Find each parasitized red blood cell.
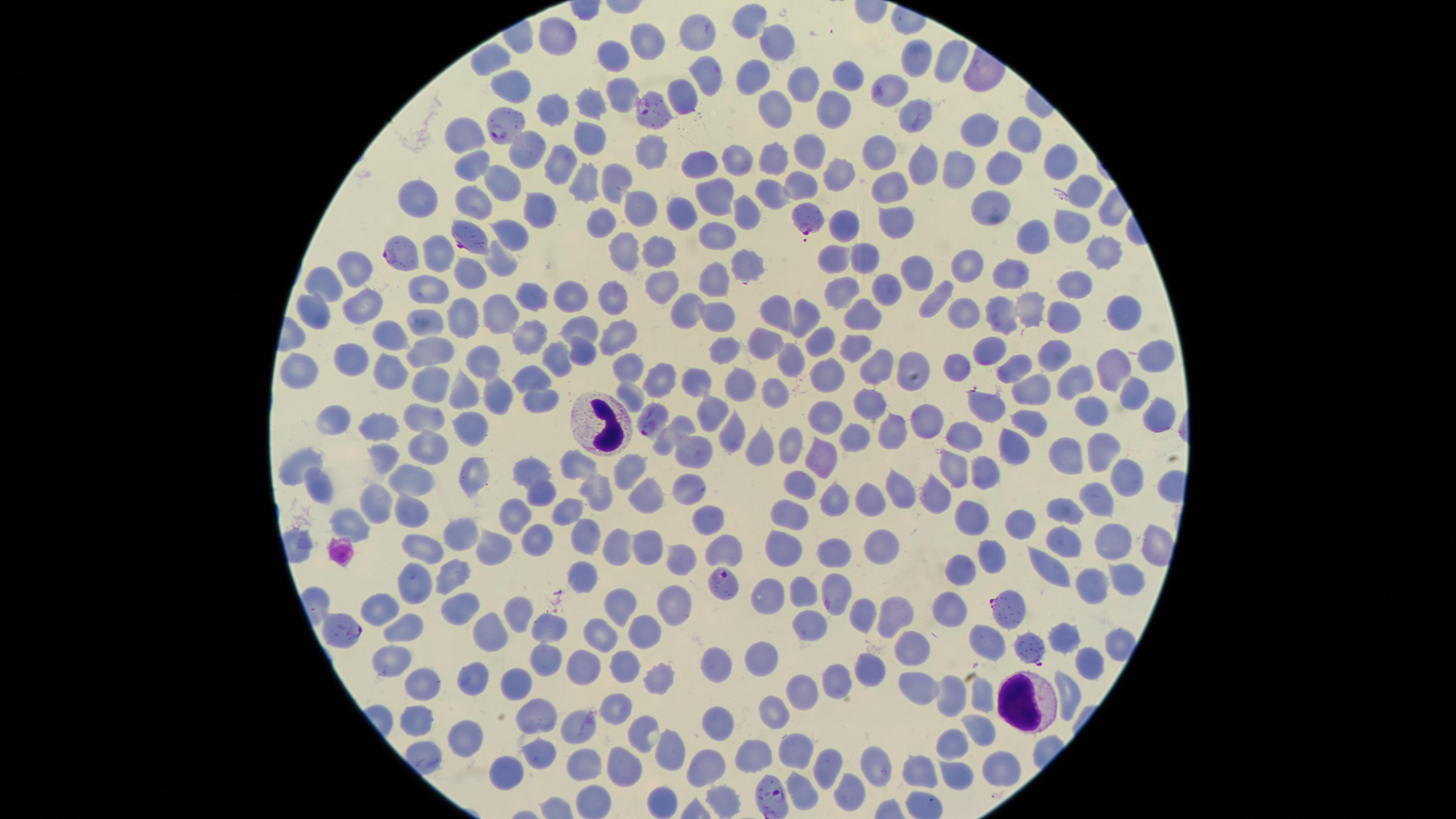

Approximate marker points as {x, y} in pixels.
Parasitized red blood cells: {654, 111}, {506, 126}, {809, 220}, {465, 234}, {397, 256}, {649, 417}, {724, 579}, {1005, 609}, {341, 628}, {1034, 645}, {774, 798}.

field of view = single
uninfected red blood cells = approximate marker points as {x, y} in pixels: {750, 15}, {695, 22}, {570, 30}, {647, 44}, {775, 45}, {489, 55}, {919, 57}, {946, 62}, {613, 63}, {708, 69}, {755, 75}, {846, 77}, {510, 82}, {808, 87}, {613, 92}, {686, 93}, {894, 93}, {587, 104}, {550, 105}, {774, 109}, {829, 110}, {914, 117}, {975, 128}, {1020, 132}, {465, 133}, {583, 139}, {877, 145}, {810, 146}, {648, 151}, {529, 153}, {999, 157}, {779, 158}, {1057, 159}, {556, 160}, {731, 161}, {469, 164}, {921, 164}, {702, 168}, {954, 168}, {836, 174}, {502, 176}, {585, 176}, {614, 176}, {885, 182}, {801, 183}, {773, 188}, {1074, 191}, {714, 198}, {419, 201}, {537, 201}, {637, 202}, {475, 204}, {993, 205}, {678, 210}, {744, 214}, {598, 220}, {896, 221}, {842, 222}, {1071, 223}, {717, 227}, {506, 232}, {1029, 238}, {622, 248}, {654, 248}, {436, 251}, {1101, 251}, {833, 254}, {868, 258}, {499, 259}, {968, 261}, {353, 266}, {743, 268}, {911, 268}, {1012, 269}, {467, 273}, {708, 276}, {327, 280}, {1076, 282}, {881, 284}, {663, 285}, {838, 289}, {429, 290}, {607, 293}, {534, 295}, {575, 296}, {939, 298}, {1034, 300}, {365, 302}, {716, 303}, {688, 306}, {314, 310}, {509, 311}, {1001, 311}, {1116, 312}, {778, 313}, {964, 313}, {460, 314}, {810, 314}, {864, 314}, {1060, 320}, {616, 326}, {425, 327}, {584, 329}, {394, 339}, {533, 339}, {758, 347}, {815, 347}, {849, 348}, {991, 349}, {580, 350}, {1052, 351}, {430, 352}, {718, 352}, {1158, 357}, {558, 359}, {354, 361}, {483, 361}, {783, 361}, {907, 362}, {959, 362}, {630, 364}, {1015, 367}, {878, 368}, {300, 369}, {1110, 371}, {387, 372}, {531, 372}, {660, 378}, {831, 378}, {429, 380}, {1081, 380}, {698, 381}, {742, 381}, {773, 384}, {1132, 391}, {1031, 392}, {463, 394}, {631, 397}, {538, 399}, {491, 400}, {873, 401}, {982, 403}, {424, 409}, {713, 409}, {1093, 411}, {335, 412}, {827, 415}, {1027, 418}, {1162, 419}, {922, 420}, {676, 425}, {469, 427}, {374, 428}, {892, 430}, {852, 433}, {965, 435}, {732, 436}, {785, 443}, {1012, 444}, {1100, 445}, {427, 447}, {693, 448}, {760, 449}, {1073, 455}, {822, 456}, {386, 457}, {299, 461}, {535, 463}, {628, 463}, {954, 466}, {580, 473}, {983, 473}, {1125, 475}, {475, 476}, {415, 480}, {323, 483}, {798, 484}, {693, 485}, {597, 490}, {644, 491}, {938, 491}, {896, 492}, {832, 493}, {541, 495}, {1097, 495}, {867, 497}, {373, 500}, {1069, 509}, {564, 511}, {786, 511}, {712, 516}, {518, 517}, {969, 517}, {1016, 520}, {347, 521}, {463, 529}, {1115, 537}, {648, 538}, {586, 539}, {535, 542}, {614, 542}, {429, 546}, {1069, 546}, {491, 547}, {873, 547}, {724, 549}, {783, 549}, {830, 549}, {989, 550}, {683, 558}, {959, 564}, {1050, 565}, {579, 570}, {452, 572}, {1119, 573}, {416, 580}, {838, 582}, {1090, 582}, {802, 586}, {768, 591}, {616, 598}, {953, 600}, {517, 603}, {672, 605}, {379, 606}, {457, 608}, {859, 612}, {890, 613}, {810, 618}, {547, 624}, {408, 625}, {486, 625}, {646, 630}, {1070, 631}, {602, 632}, {987, 642}, {1109, 646}, {918, 652}, {764, 655}, {541, 658}, {392, 661}, {715, 661}, {579, 662}, {1084, 662}, {631, 664}, {867, 666}, {661, 673}, {475, 674}, {517, 679}, {426, 681}, {828, 684}, {798, 688}, {924, 689}, {982, 693}, {951, 695}, {1069, 695}, {614, 707}, {772, 708}, {534, 716}, {420, 718}, {581, 726}, {640, 728}, {710, 728}, {975, 728}, {469, 738}, {954, 744}, {663, 746}, {541, 750}, {754, 752}, {794, 752}, {700, 764}, {998, 764}, {625, 765}, {830, 765}, {880, 769}, {500, 770}, {585, 770}, {917, 772}, {954, 774}, {797, 782}, {848, 789}, {720, 796}, {665, 803}
visible region = circular
capture = smartphone photograph through the microscope eyepiece
stain = Giemsa
white blood cells = approximate marker points as {x, y} in pixels: {598, 423}, {1024, 702}
preparation = thin blood smear
image size = 1456×819 pixels
species = Plasmodium falciparum